Name the parasite shown.
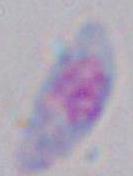
Toxoplasma gondii.

magnification = 1000x
modality = micrograph